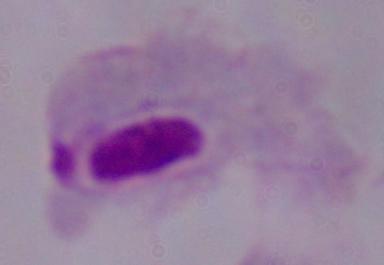

A trichomonad is seen. Micrograph. Captured at 1000x magnification.